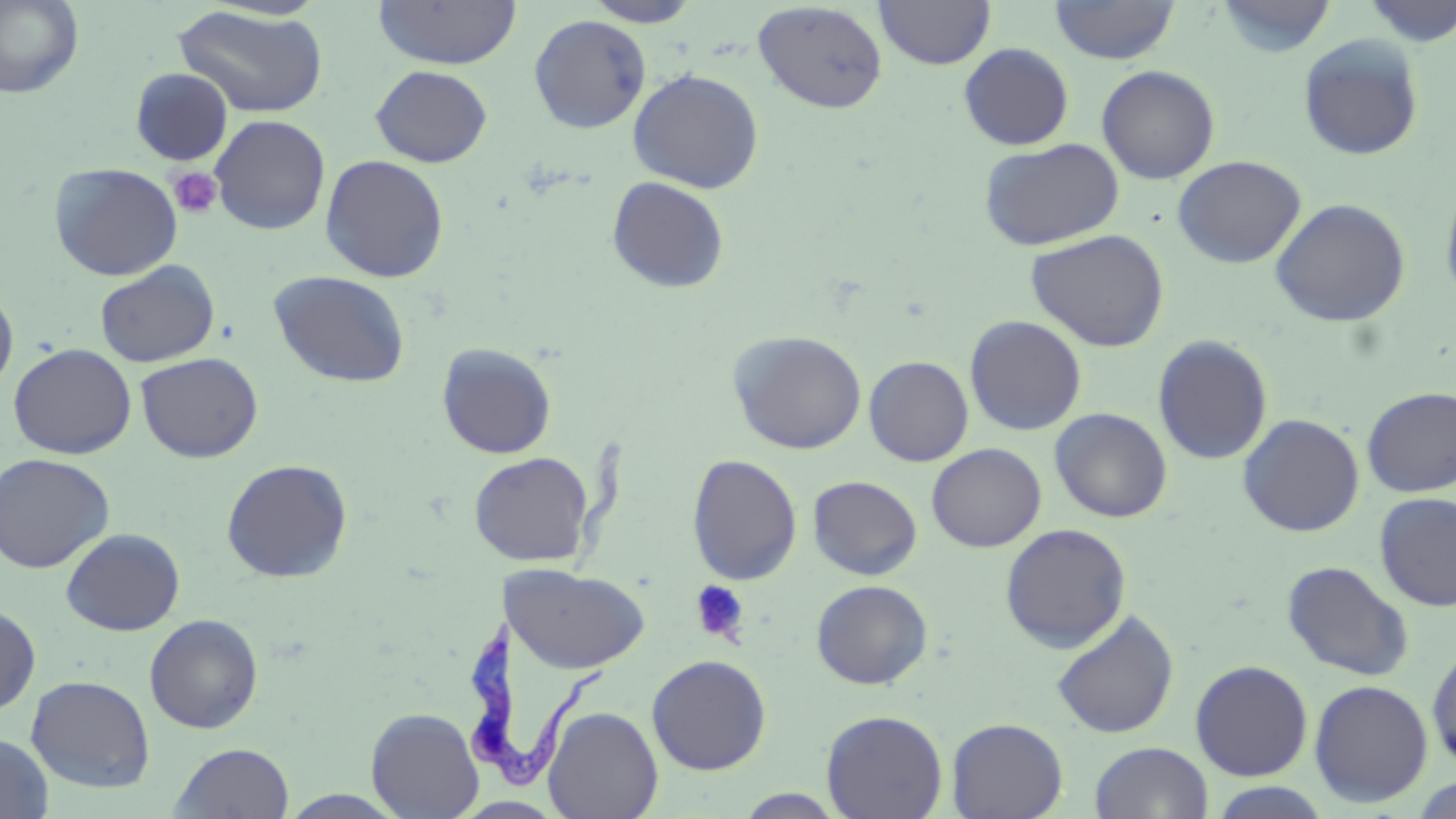 Approximate bounding boxes as [x1, y1, x2, y2] in pixels. Uninfected red blood cell locations: [373, 0, 522, 70], [583, 0, 702, 27], [874, 0, 996, 70], [1214, 0, 1337, 58], [1361, 0, 1456, 46], [0, 1, 83, 98], [752, 1, 888, 113], [1050, 1, 1179, 65], [173, 5, 328, 119], [529, 14, 651, 134], [1298, 34, 1424, 160], [958, 43, 1074, 150], [371, 65, 493, 167], [1097, 65, 1220, 184], [130, 68, 233, 165], [628, 68, 765, 193], [210, 114, 330, 235], [978, 137, 1124, 251], [320, 154, 449, 283], [1173, 155, 1306, 269], [49, 162, 183, 281], [606, 176, 730, 294], [1439, 176, 1456, 309], [1271, 198, 1411, 327], [1026, 229, 1169, 352], [95, 261, 220, 368], [268, 270, 411, 388], [0, 285, 18, 397], [964, 315, 1087, 436], [728, 331, 867, 454], [1152, 335, 1273, 465], [8, 343, 136, 459], [437, 343, 557, 459], [135, 352, 263, 463], [864, 355, 973, 466], [1361, 387, 1456, 497], [1049, 407, 1172, 523], [1238, 413, 1365, 536], [927, 443, 1047, 552], [469, 451, 594, 566], [0, 453, 115, 573], [687, 453, 803, 585], [221, 459, 353, 583], [808, 475, 922, 580], [1374, 492, 1456, 612], [1000, 523, 1131, 653], [61, 528, 185, 636], [1281, 560, 1415, 682], [506, 565, 649, 674], [810, 580, 933, 690], [0, 603, 40, 716], [1050, 609, 1179, 739], [144, 614, 264, 733], [1427, 645, 1456, 770], [646, 654, 772, 775], [1190, 660, 1313, 781], [26, 675, 155, 793], [1308, 679, 1434, 807], [542, 705, 664, 819], [366, 706, 484, 819], [821, 709, 948, 819], [946, 717, 1068, 819], [0, 732, 54, 818], [170, 742, 295, 819], [1090, 742, 1213, 819], [1410, 774, 1456, 818], [733, 789, 849, 818], [278, 790, 409, 818]. Platelet locations: [168, 167, 223, 219], [690, 579, 751, 645]. Trypanosoma brucei locations: [462, 620, 611, 790]. Slide-level diagnosis: Trypanosoma brucei. Optical microscopy. 1000x magnification. May-Grünwald-Giemsa-stained preparation. One field of a larger specimen. Thin blood smear. Image is 1456×819 pixels.